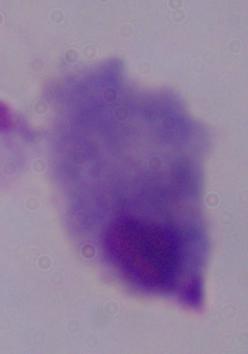

Summary:
  - Identification: trichomonad
  - Modality: micrograph
  - Magnification: 1000x